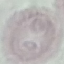
malaria status = uninfected
capture = smartphone through the microscope eyepiece
preparation = thin blood film
image type = cell patch, automatically extracted from a larger field of view and resized to 64 × 64 pixels
stain = Giemsa